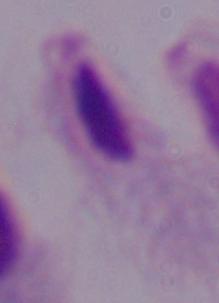

Summary:
  - Magnification: 1000x
  - Modality: micrograph
  - Identification: trichomonad